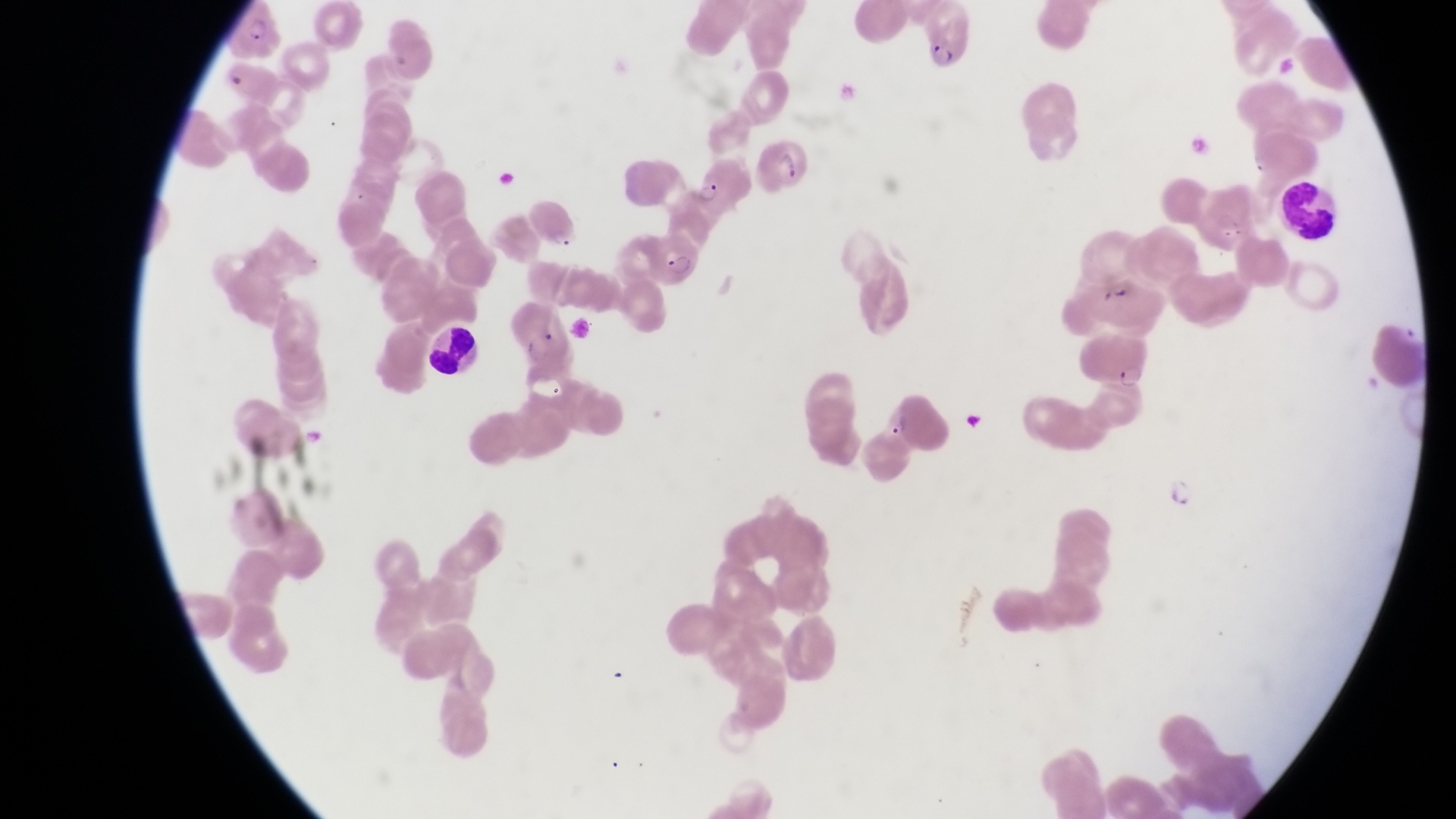
Approximate bounding boxes as [left, top, right, bottom] in pixels.
Summary:
  - Trophozoite locations: [1113, 362, 1147, 395], [880, 404, 913, 441], [1166, 473, 1203, 513]
  - Leukocyte locations: [1279, 179, 1346, 246]
  - Parasitised red blood cell locations: [922, 6, 982, 82], [227, 7, 285, 67], [756, 133, 814, 191], [692, 153, 752, 212], [651, 230, 706, 293], [422, 320, 486, 383]
  - Preparation: thin blood smear
  - Country: Uganda
  - Image size: 1456×819 pixels
  - Magnification: 1000x
  - Capture: smartphone photograph through the eyepiece of an Olympus CX-23 microscope
  - Field of view: single